Assess the morphology of the erythrocytes.
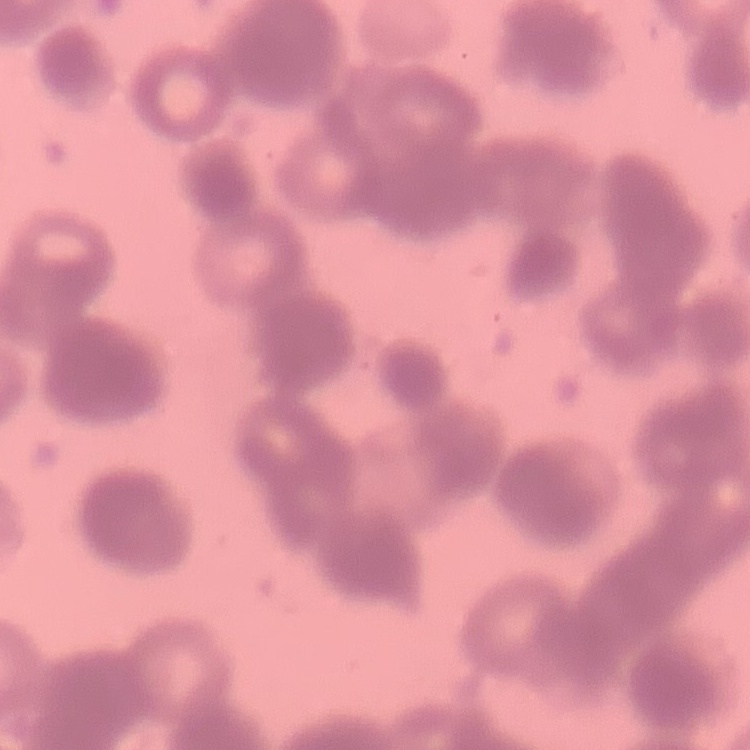

Rouleaux formation.

Summary:
  - Stain: Field's or Giemsa
  - Preparation: thin blood film
  - Image type: one tile cut from a larger photomicrograph